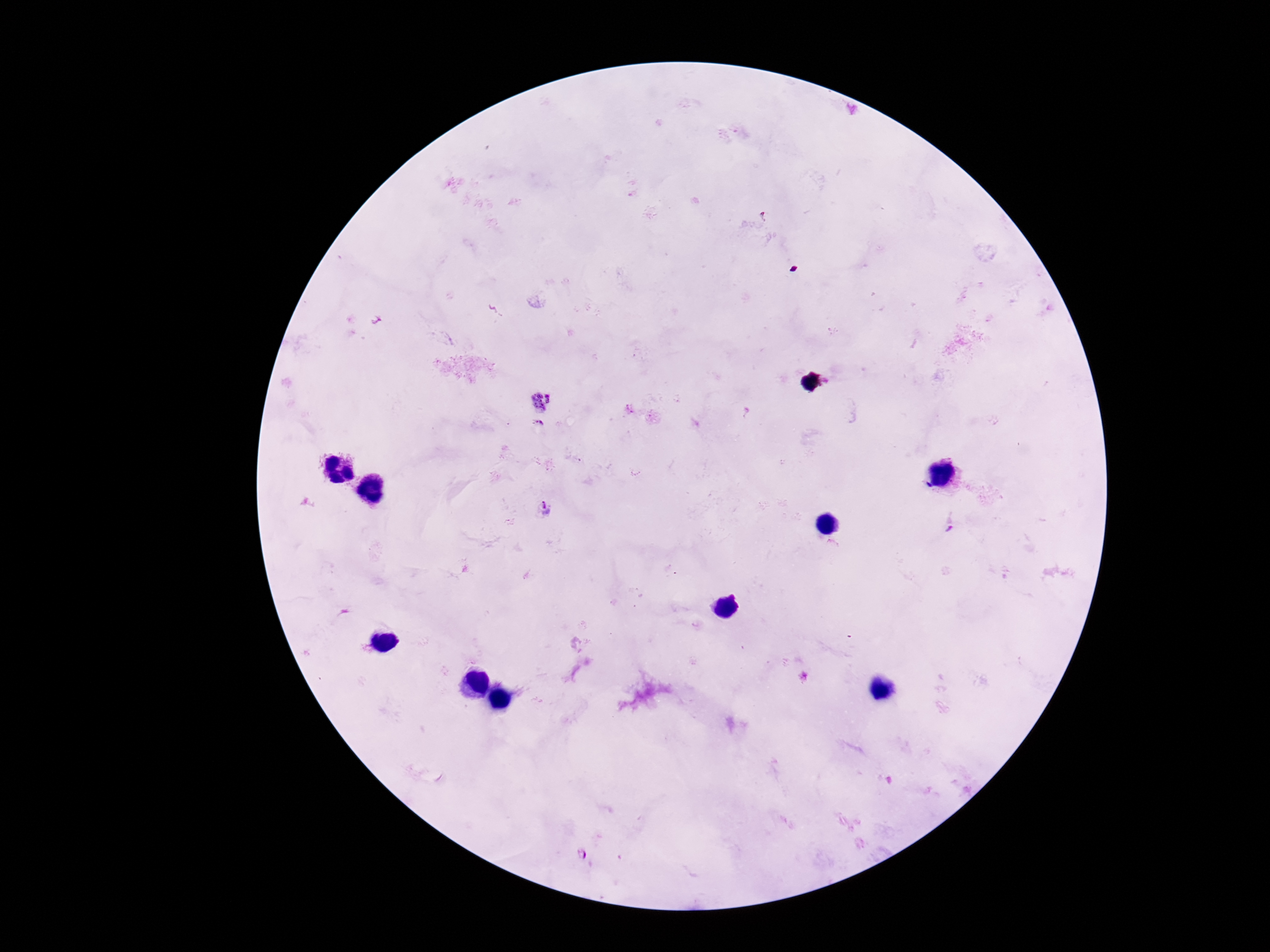
Approximate centers as {x, y} in pixels.
Summary:
  - Plasmodium parasite locations: {765, 217}, {541, 400}, {632, 408}, {540, 425}, {548, 510}, {950, 522}, {582, 856}
  - Patient malaria status: positive
  - Preparation: thick blood smear
  - Field of view: single
  - Magnification: 100x
  - Capture: smartphone camera through the microscope eyepiece
  - Stain: Giemsa
  - Image size: 1270×952 pixels